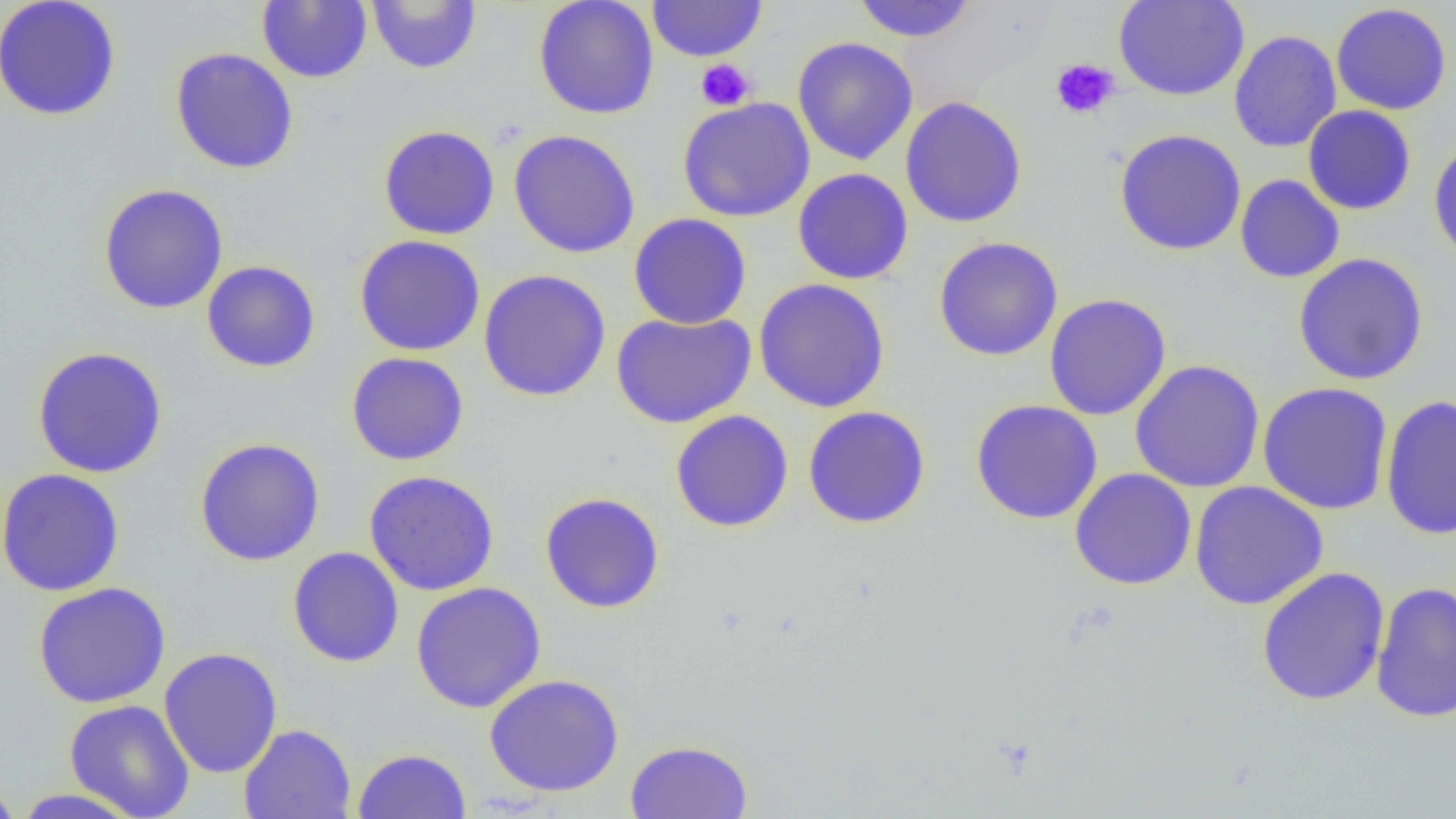
Summary:
  - Coordinate format: approximate bounding boxes as (x1, y1, x2, y2) in pixels
  - Platelet locations: (695, 58, 756, 111), (1050, 58, 1120, 120)
  - Uninfected red blood cell locations: (0, 0, 122, 122), (367, 0, 481, 74), (533, 0, 660, 120), (1113, 0, 1249, 101), (257, 1, 372, 83), (647, 1, 766, 62), (851, 1, 978, 43), (1331, 3, 1452, 115), (1228, 30, 1341, 153), (792, 36, 919, 166), (169, 47, 299, 175), (900, 96, 1028, 228), (676, 97, 815, 222), (1303, 104, 1417, 215), (377, 124, 501, 240), (1114, 128, 1246, 256), (508, 129, 641, 258), (1428, 136, 1456, 267), (793, 168, 913, 284), (1235, 174, 1345, 283), (97, 183, 229, 314), (628, 212, 752, 330), (354, 235, 486, 357), (932, 236, 1064, 361), (1292, 253, 1429, 385), (202, 260, 320, 373), (478, 269, 611, 401), (753, 278, 891, 413), (1044, 293, 1172, 421), (611, 310, 756, 428), (31, 346, 168, 478), (345, 352, 469, 466), (1129, 359, 1265, 493), (1257, 382, 1393, 515), (1379, 394, 1456, 540), (969, 399, 1103, 524), (802, 405, 931, 529), (670, 410, 793, 532), (194, 437, 325, 566), (0, 468, 125, 596), (1069, 468, 1197, 590), (364, 470, 500, 595), (1189, 481, 1329, 610), (539, 492, 666, 614), (287, 547, 404, 668), (1256, 566, 1391, 706), (1370, 580, 1456, 723), (32, 581, 171, 708), (410, 581, 547, 714), (158, 646, 283, 778), (484, 673, 624, 797), (64, 699, 196, 819), (239, 724, 357, 819), (624, 739, 754, 819), (353, 748, 471, 819), (0, 776, 22, 819), (9, 788, 146, 818)
  - Slide-level diagnosis: negative for blood parasites
  - Magnification: 1000x
  - Image size: 1456×819 pixels
  - Field of view: single
  - Preparation: thin blood smear
  - Modality: optical microscopy